Assess for Plasmodium parasites.
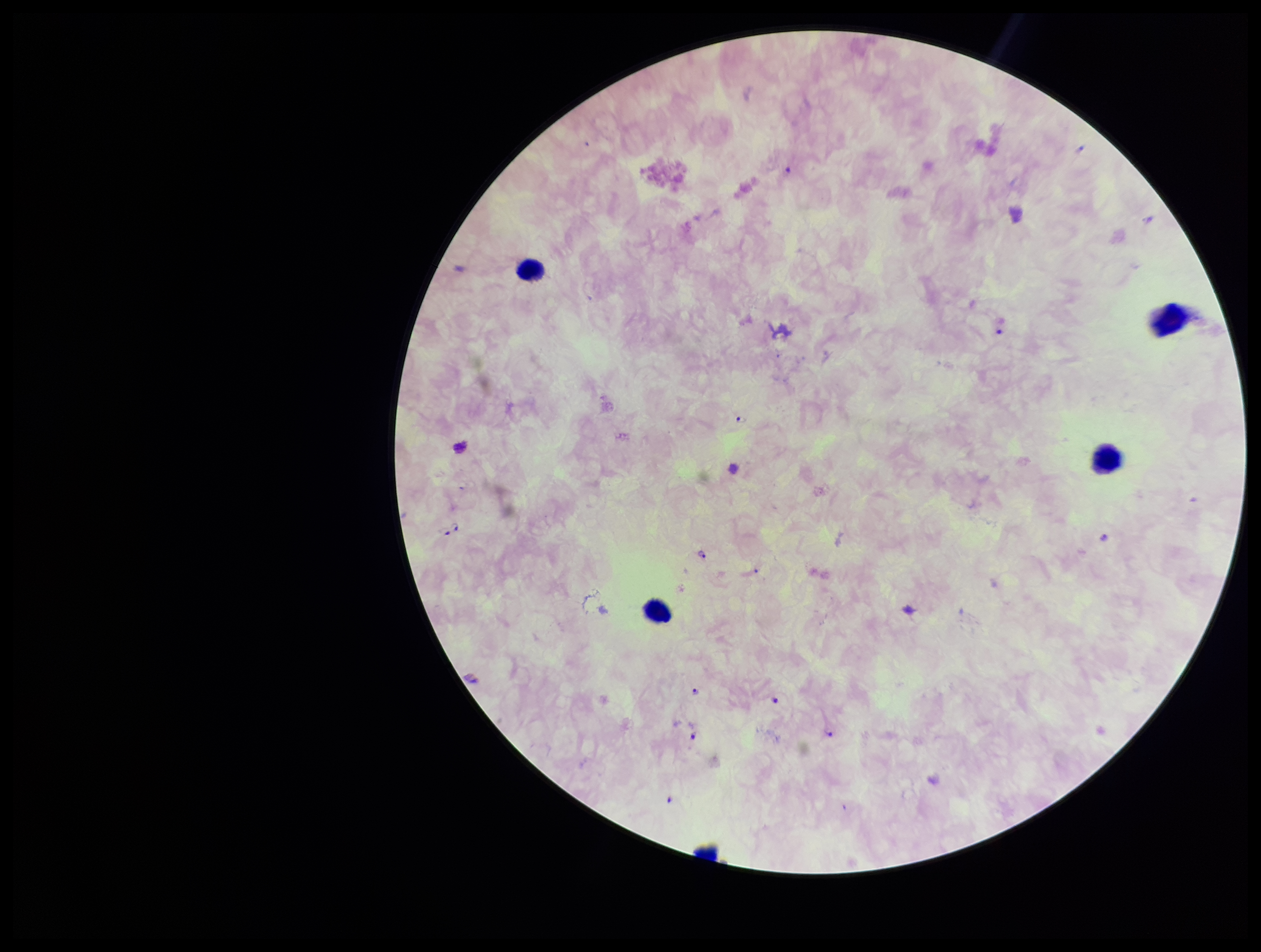

Seen.

species reported for this patient = Plasmodium falciparum
stain = Giemsa
leukocyte count = 4
patient malaria status = positive
field of view = one from this slide
parasite count = 7
capture = smartphone photograph through the microscope eyepiece
image size = 1261×952 pixels
preparation = thick blood smear